State which cell type is depicted.
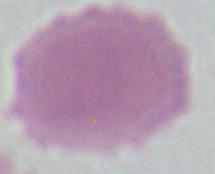
An erythrocyte.

magnification = 1000x
modality = micrograph